Classify this cell by malaria status.
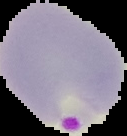

Parasitized.

Summary:
  - Preparation: thin blood smear
  - Image size: 127×136 pixels
  - Image type: segmented cell region with the area outside set to black